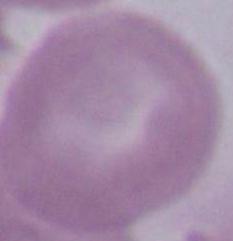

magnification: 1000x
identification: red blood cell
modality: micrograph